Describe the morphology of the erythrocytes.
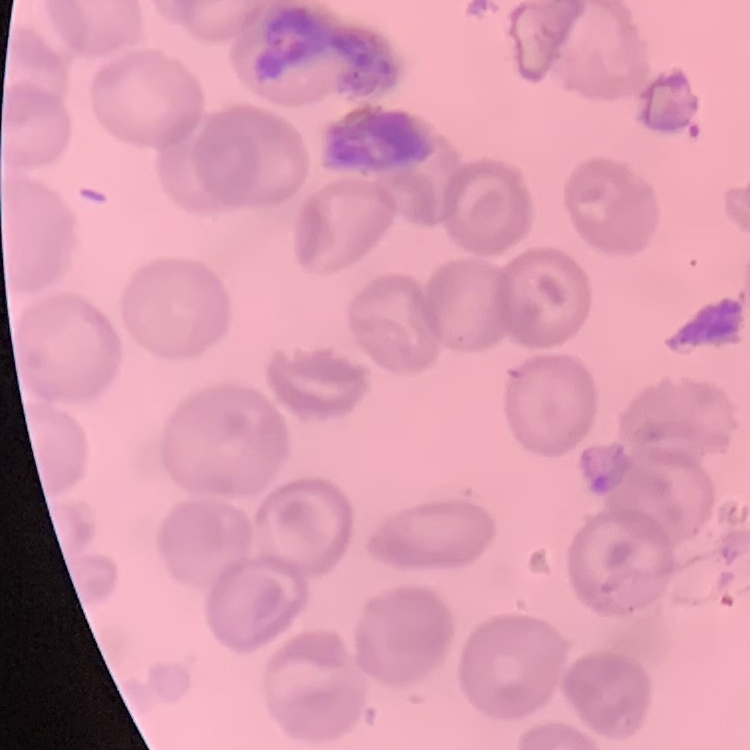

No rouleaux formation.

One tile cut from a larger photomicrograph. Thin blood film. Field's or Giemsa stain.